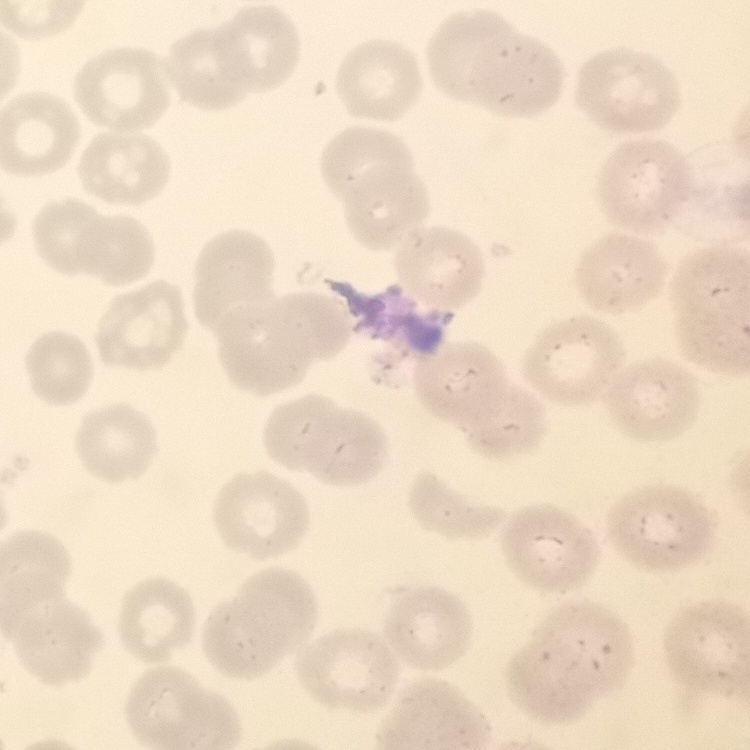
The erythrocytes show no rouleaux formation. One tile cut from a larger photomicrograph. Stained with either Field's or Giemsa. Thin blood film.